Describe the morphology of the erythrocytes.
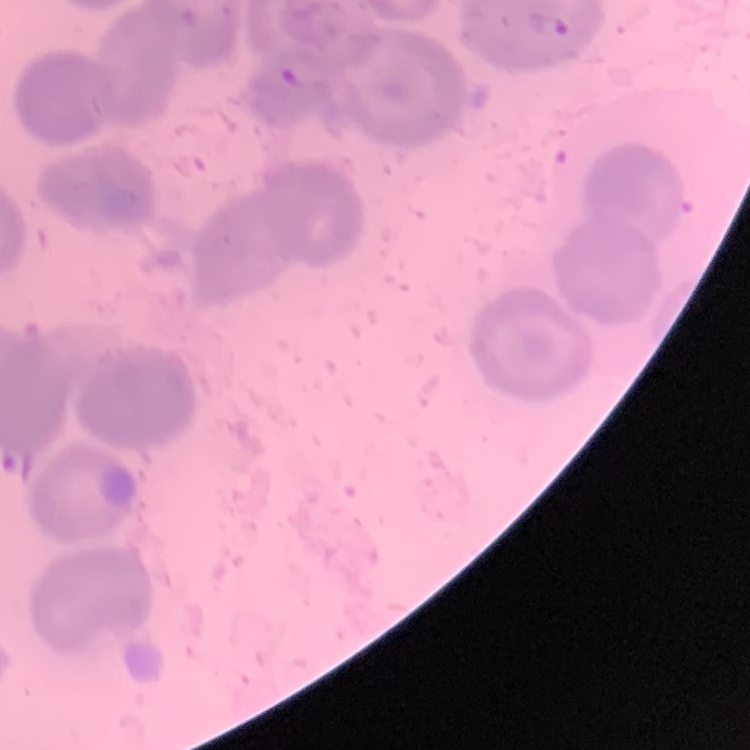

They show no rouleaux formation.

stain = Field's or Giemsa
image type = square crop of a larger photomicrograph
preparation = thin blood smear